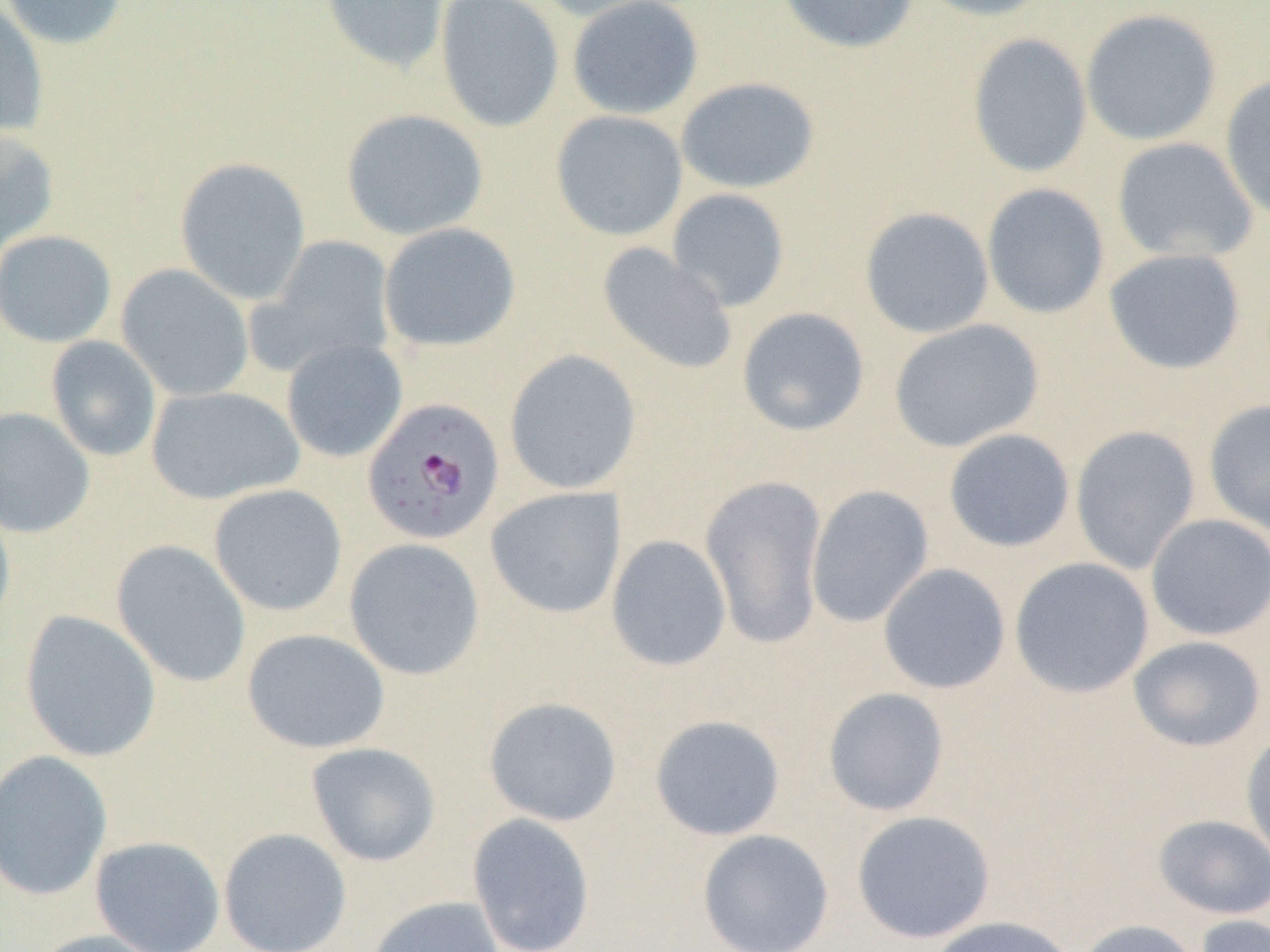
slide-level diagnosis = Plasmodium falciparum
image size = 1270×952 pixels
uninfected red blood cell locations = approximate bounding boxes as (x1,y1)-(x2,y2) corner pairs in pixels: (0,0)-(128,50), (321,0)-(450,76), (434,0)-(564,133), (528,0)-(681,23), (566,0)-(705,120), (776,0)-(919,54), (910,0)-(1053,22), (0,3)-(49,138), (1080,8)-(1222,146), (967,33)-(1092,179), (1219,74)-(1270,224), (675,77)-(821,194), (340,108)-(489,241), (550,110)-(688,242), (0,129)-(60,256), (1110,137)-(1258,264), (174,156)-(311,305), (981,182)-(1110,319), (666,188)-(790,312), (859,207)-(995,339), (378,221)-(521,353), (0,229)-(117,348), (253,234)-(397,376), (597,242)-(738,376), (1103,247)-(1247,375), (116,264)-(254,402), (736,307)-(870,437), (888,318)-(1044,453), (45,336)-(163,462), (281,338)-(408,463), (504,349)-(642,495), (145,385)-(305,504), (1203,399)-(1270,535), (0,407)-(95,538), (1070,424)-(1201,575), (943,428)-(1075,553), (699,473)-(829,650), (208,484)-(348,616), (806,484)-(935,628), (485,486)-(626,619), (0,493)-(16,638), (1145,513)-(1270,641), (605,534)-(732,672), (343,538)-(486,680), (111,540)-(251,688), (1009,556)-(1155,698), (877,563)-(1011,694), (18,610)-(162,763), (240,628)-(391,754), (1127,635)-(1266,752), (822,687)-(950,817), (483,696)-(624,826), (649,714)-(786,841), (1240,730)-(1270,867), (305,742)-(442,867), (0,749)-(113,901), (851,810)-(996,944), (466,812)-(597,952), (1152,814)-(1270,919), (218,827)-(352,952), (696,829)-(834,952), (89,835)-(226,952), (364,895)-(504,952), (1193,914)-(1270,952), (929,916)-(1076,952), (1072,918)-(1202,952), (27,929)-(172,952)
Plasmodium falciparum-infected red blood cell locations = approximate bounding boxes as (x1,y1)-(x2,y2) corner pairs in pixels: (361,398)-(506,546)
modality = optical microscopy
magnification = 1000x
preparation = thin blood smear
field of view = single